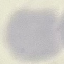
Summary:
  - Result: negative for malaria parasites
  - Preparation: thin blood smear
  - Stain: Giemsa
  - Image type: cell patch, automatically extracted from a larger field of view and resized to 64 × 64 pixels
  - Capture: smartphone through the microscope eyepiece